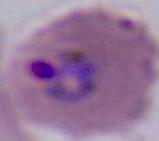

A Plasmodium parasite is shown. Photomicrograph. 400x or 1000x magnification.